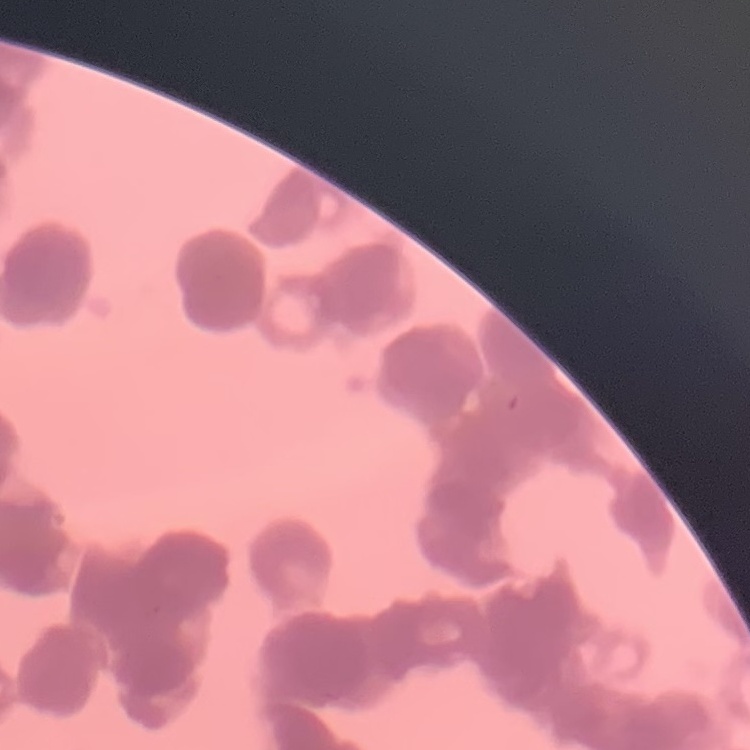
red blood cell morphology = rouleaux formation
preparation = thin blood smear
stain = Field's or Giemsa
image type = one tile cut from a larger photomicrograph